Outline each blood parasite and name the species.
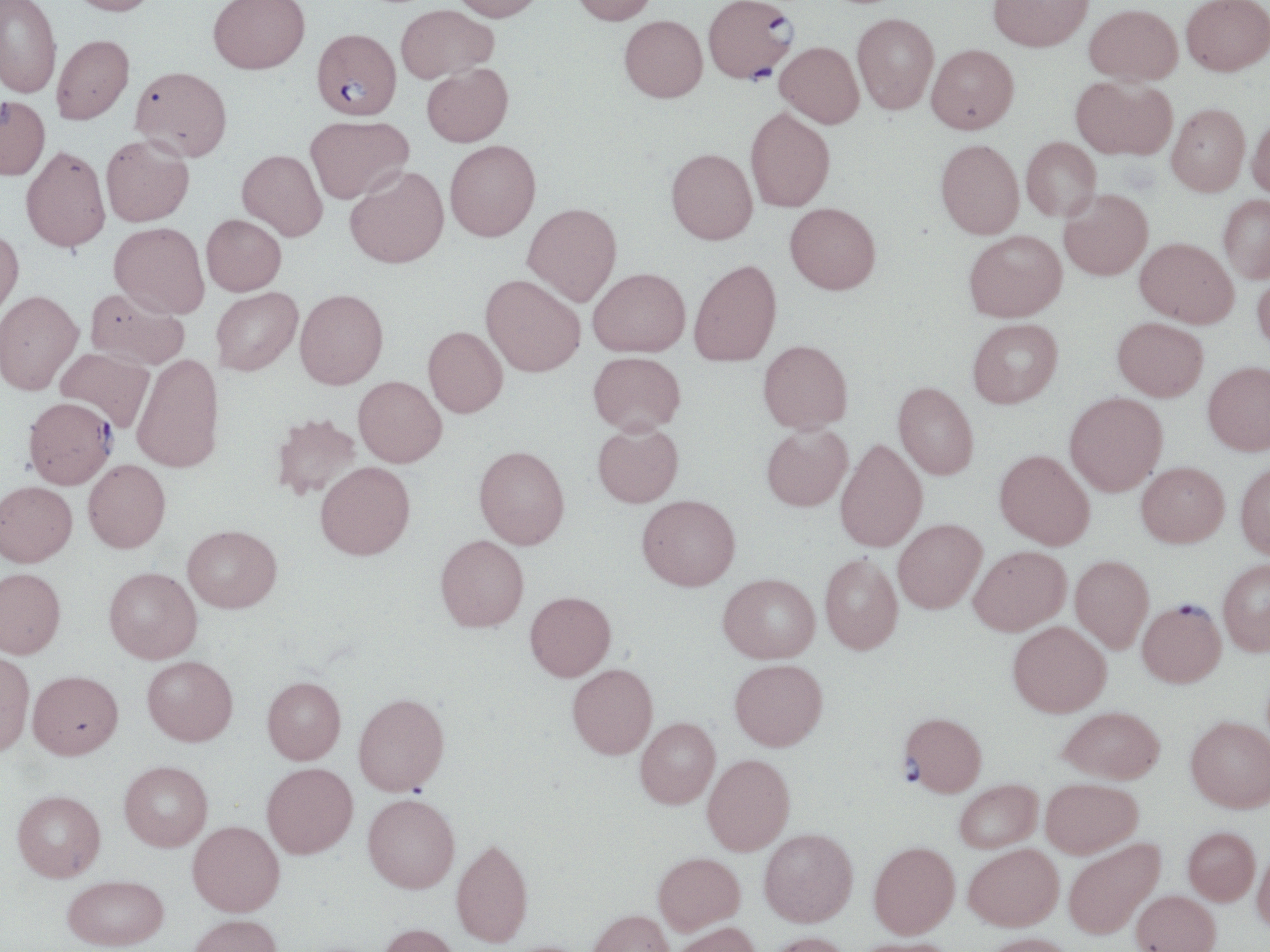

Approximate bounding boxes as [x1, y1, x2, y2] in pixels.
Plasmodium falciparum-infected red blood cells: [704, 2, 797, 83], [312, 28, 400, 120], [22, 396, 117, 488], [1137, 599, 1225, 686], [899, 712, 987, 796].
No Plasmodium ovale, Plasmodium malariae, Plasmodium vivax, Babesia divergens, or Trypanosoma brucei observed.

Uninfected red blood cell locations: [0, 0, 61, 99], [68, 0, 160, 17], [208, 0, 310, 73], [451, 0, 546, 21], [570, 0, 658, 25], [988, 0, 1093, 51], [1182, 0, 1270, 76], [395, 4, 497, 83], [1085, 4, 1183, 85], [852, 13, 939, 114], [619, 15, 707, 103], [52, 34, 135, 124], [776, 41, 864, 128], [927, 44, 1019, 133], [422, 63, 513, 147], [130, 66, 232, 162], [1071, 76, 1176, 160], [0, 96, 50, 180], [1167, 103, 1250, 195], [745, 107, 835, 212], [1248, 114, 1270, 199], [305, 115, 413, 204], [101, 135, 194, 227], [1021, 137, 1101, 221], [935, 139, 1024, 239], [445, 140, 540, 241], [21, 146, 110, 252], [666, 148, 757, 244], [237, 149, 328, 240], [345, 166, 449, 268], [1059, 189, 1153, 280], [1218, 195, 1270, 283], [785, 202, 881, 294], [522, 203, 621, 306], [201, 214, 286, 295], [109, 222, 209, 318], [0, 228, 24, 319], [964, 230, 1067, 321], [1135, 237, 1239, 327], [689, 260, 781, 366], [588, 268, 690, 357], [1252, 273, 1270, 354], [481, 274, 585, 376], [85, 288, 189, 370], [211, 288, 302, 375], [0, 289, 83, 395], [295, 289, 388, 389], [1113, 317, 1208, 401], [968, 318, 1063, 407], [423, 326, 507, 417], [758, 340, 853, 433], [55, 347, 155, 431], [588, 351, 685, 434], [132, 354, 224, 473], [1203, 361, 1270, 455], [353, 376, 446, 467], [893, 382, 979, 479], [1065, 393, 1167, 495], [271, 412, 362, 502], [592, 423, 683, 507], [761, 424, 852, 511], [835, 438, 927, 552], [474, 445, 569, 549], [995, 449, 1095, 549], [83, 459, 170, 552], [1235, 461, 1270, 559], [315, 462, 415, 560], [1137, 462, 1229, 547], [0, 481, 77, 566], [637, 494, 740, 590], [893, 518, 986, 613], [182, 525, 282, 613], [435, 535, 529, 632], [969, 545, 1070, 635], [820, 554, 903, 654], [1070, 555, 1154, 653], [1218, 558, 1270, 655], [0, 567, 65, 658], [104, 567, 202, 663], [718, 573, 820, 663], [525, 591, 615, 681], [1008, 621, 1111, 717], [0, 650, 35, 756], [142, 656, 238, 746], [730, 659, 828, 750], [567, 663, 657, 759], [28, 670, 123, 759], [262, 676, 346, 763], [353, 692, 450, 796], [1059, 706, 1165, 783], [1186, 716, 1270, 812], [635, 718, 720, 808], [702, 754, 795, 854], [119, 761, 213, 851], [262, 762, 358, 858], [1041, 777, 1142, 857], [954, 779, 1042, 852], [12, 789, 106, 881], [363, 794, 460, 893], [188, 821, 284, 916], [1183, 827, 1260, 904], [759, 828, 858, 926], [451, 838, 533, 947], [1063, 838, 1165, 939], [869, 841, 959, 938], [964, 843, 1063, 930], [1253, 846, 1270, 932], [653, 852, 745, 934], [63, 874, 168, 950], [1131, 890, 1221, 952], [588, 910, 675, 952], [188, 914, 281, 952], [671, 921, 759, 952], [377, 923, 461, 952], [766, 932, 854, 952], [982, 933, 1077, 952], [850, 937, 958, 952]. Slide-level diagnosis: Plasmodium falciparum. Captured at 1000x magnification. Image is 1270×952 pixels. May-Grünwald-Giemsa stain. Single field of view. Thin blood film. Light microscopy.